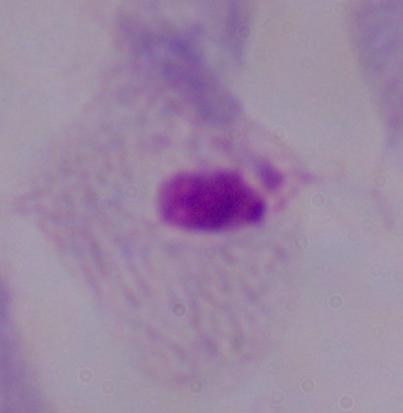 Captured at 1000x magnification. Micrograph. A trichomonad is shown.